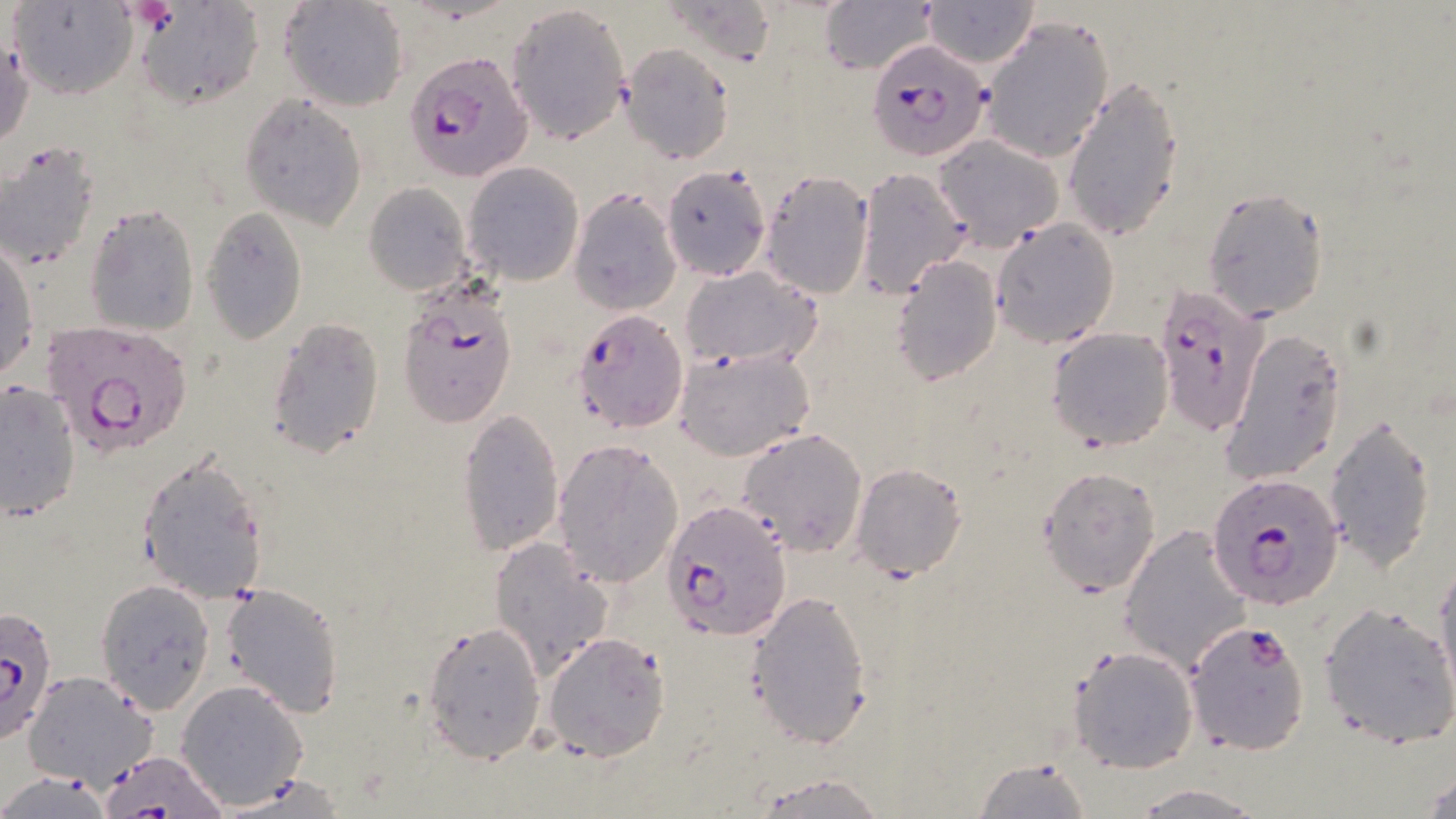
{
  "slide_level_diagnosis": "Plasmodium falciparum",
  "preparation": "thin blood film",
  "plasmodium_falciparum_infected_red_blood_cell_locations": "approximate bounding boxes as [x1, y1, x2, y2] in pixels: [870, 37, 992, 164], [404, 50, 533, 182], [1152, 282, 1269, 438], [399, 284, 516, 430], [570, 307, 689, 434], [42, 318, 194, 460], [1208, 473, 1341, 612], [662, 500, 792, 643], [0, 605, 59, 744], [1195, 617, 1322, 753]",
  "magnification": "1000x",
  "image_size": "1456×819 pixels",
  "uninfected_red_blood_cell_locations": "approximate bounding boxes as [x1, y1, x2, y2] in pixels: [11, 0, 139, 100], [280, 0, 408, 112], [922, 0, 1039, 67], [135, 1, 263, 107], [817, 1, 938, 76], [508, 3, 634, 145], [980, 15, 1114, 163], [1, 35, 33, 151], [619, 43, 735, 196], [1062, 74, 1184, 243], [239, 94, 368, 230], [936, 134, 1065, 249], [0, 142, 100, 270], [462, 162, 584, 286], [661, 165, 771, 281], [855, 166, 974, 301], [759, 170, 875, 298], [364, 182, 474, 297], [568, 188, 681, 314], [1202, 188, 1331, 322], [84, 205, 199, 336], [200, 208, 308, 342], [990, 219, 1120, 348], [0, 241, 37, 382], [889, 254, 1004, 386], [681, 266, 821, 368], [264, 315, 386, 461], [1047, 328, 1174, 451], [1219, 330, 1349, 487], [674, 346, 816, 461], [0, 378, 81, 523], [456, 409, 564, 556], [1323, 412, 1440, 571], [736, 427, 869, 557], [552, 437, 684, 587], [135, 453, 269, 603], [849, 463, 967, 582], [1037, 467, 1162, 595], [1120, 525, 1251, 676], [489, 534, 614, 681], [1431, 553, 1456, 705], [95, 579, 216, 712], [221, 583, 344, 718], [747, 589, 874, 749], [1317, 602, 1456, 750], [422, 619, 546, 763], [542, 632, 672, 761], [1067, 645, 1199, 774], [24, 671, 157, 789], [176, 679, 307, 810], [105, 748, 222, 817], [976, 757, 1092, 817], [1422, 767, 1456, 818], [1, 772, 115, 818], [755, 773, 888, 816], [1131, 784, 1262, 816]",
  "stain": "May-Grünwald-Giemsa",
  "field_of_view": "one of a larger specimen",
  "modality": "light microscopy"
}